Describe the morphology of the red blood cells.
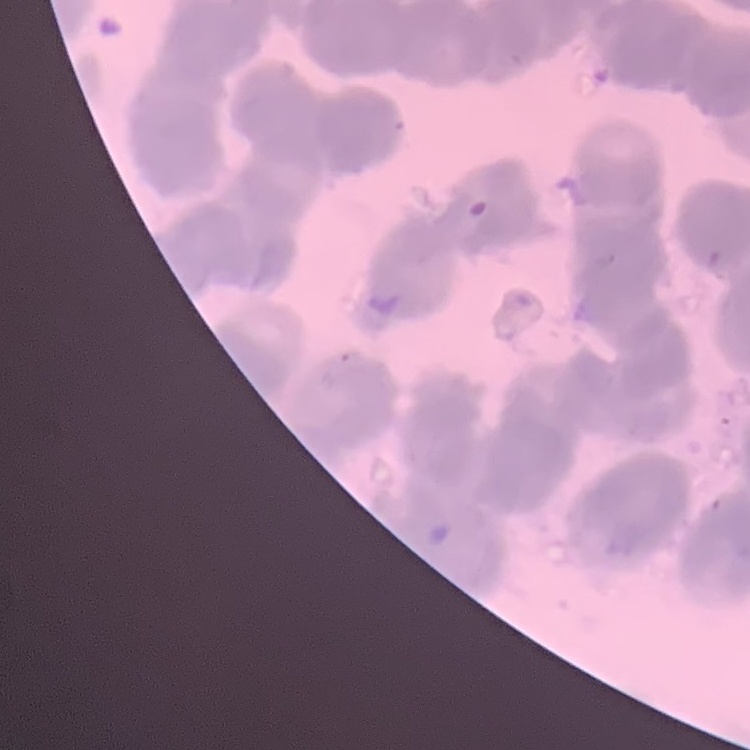

Rouleaux formation.

Summary:
  - Stain: Field's or Giemsa
  - Preparation: thin blood smear
  - Image type: one tile cut from a larger photomicrograph